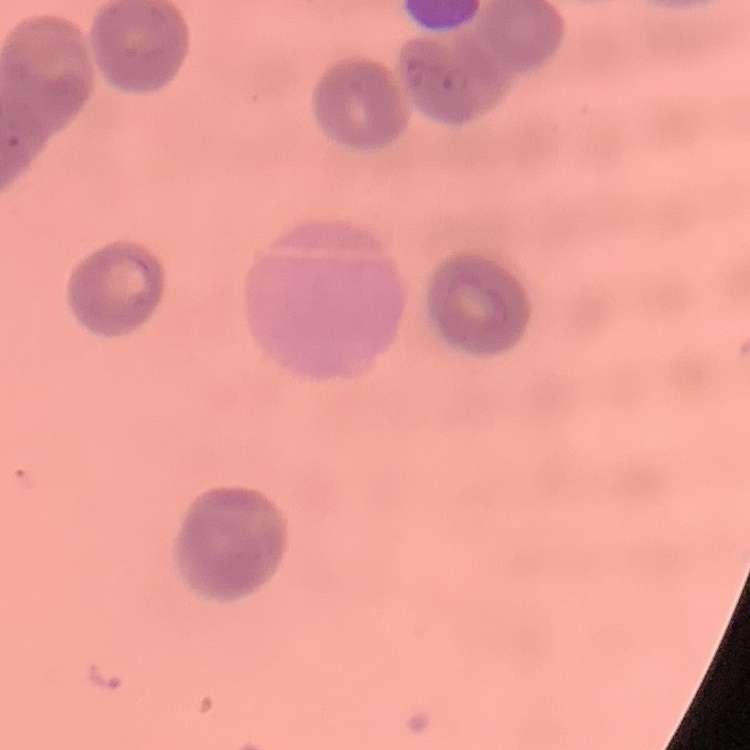

Summary:
  - Erythrocyte morphology: rouleaux formation
  - Image type: square crop of a larger photomicrograph
  - Stain: Field's or Giemsa
  - Preparation: thin blood smear